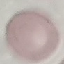
Malaria status: uninfected. Thin blood smear. Giemsa-stained preparation. Cell patch, automatically extracted from a larger field of view and resized to 64 × 64 pixels. Acquired by smartphone through the microscope eyepiece.